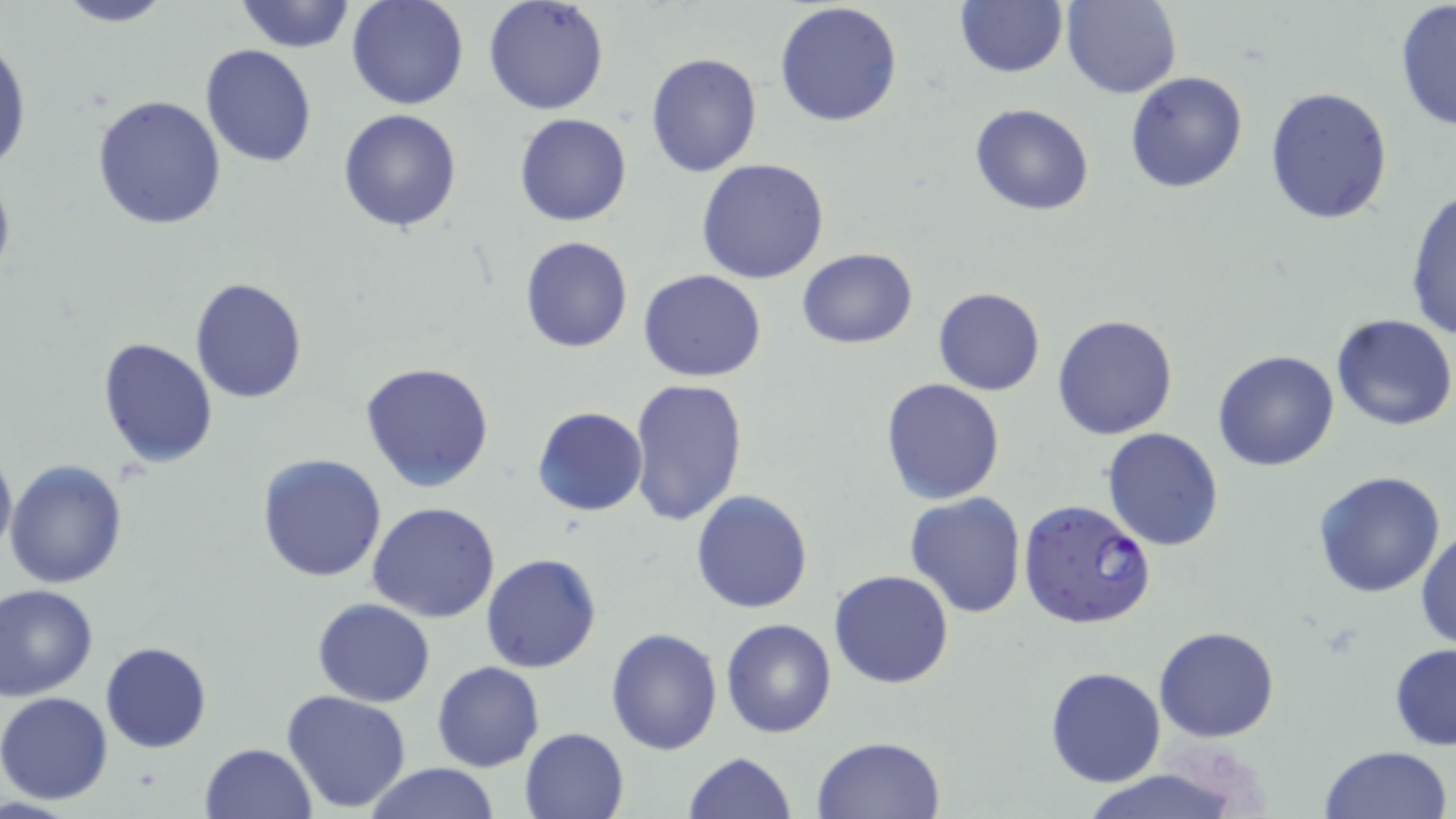

Summary:
  - Coordinate format: approximate bounding boxes as (x1, y1, x2, y2) in pixels
  - Plasmodium falciparum-infected red blood cell locations: (1017, 498, 1157, 630)
  - Uninfected red blood cell locations: (51, 0, 176, 27), (234, 0, 356, 54), (345, 0, 469, 112), (482, 0, 611, 116), (1061, 0, 1181, 99), (773, 1, 903, 128), (954, 2, 1068, 78), (1395, 2, 1456, 134), (0, 36, 32, 177), (201, 44, 317, 168), (645, 51, 763, 176), (1125, 71, 1248, 193), (1265, 87, 1394, 224), (90, 94, 227, 231), (970, 104, 1095, 216), (337, 107, 463, 234), (514, 113, 632, 227), (695, 159, 830, 284), (0, 167, 16, 288), (1403, 187, 1456, 343), (519, 235, 632, 354), (795, 248, 918, 350), (638, 268, 767, 382), (189, 278, 308, 404), (933, 287, 1045, 396), (1331, 313, 1456, 431), (1051, 314, 1178, 440), (97, 337, 218, 467), (1212, 348, 1340, 471), (360, 360, 495, 493), (879, 377, 1005, 505), (626, 378, 746, 529), (532, 406, 649, 516), (1101, 427, 1225, 550), (0, 438, 16, 563), (256, 453, 388, 582), (6, 459, 128, 590), (1312, 470, 1446, 597), (690, 490, 812, 613), (904, 493, 1027, 618), (367, 502, 502, 623), (1414, 523, 1456, 653), (480, 553, 602, 673), (829, 569, 954, 688), (0, 583, 97, 701), (313, 598, 436, 707), (721, 618, 837, 737), (1154, 625, 1280, 743), (606, 627, 722, 755), (100, 641, 212, 753), (1389, 644, 1456, 751), (432, 661, 544, 772), (1045, 667, 1165, 787), (282, 688, 413, 812), (0, 691, 115, 805), (519, 727, 629, 819), (811, 735, 946, 818), (198, 742, 318, 819), (1318, 745, 1452, 819), (685, 751, 795, 819), (361, 762, 499, 819), (1076, 766, 1246, 819)
  - Slide-level diagnosis: Plasmodium falciparum
  - Field of view: one of a larger specimen
  - Image size: 1456×819 pixels
  - Preparation: thin blood film
  - Stain: May-Grünwald-Giemsa
  - Modality: light microscopy
  - Magnification: 1000x